Give the preparation type.
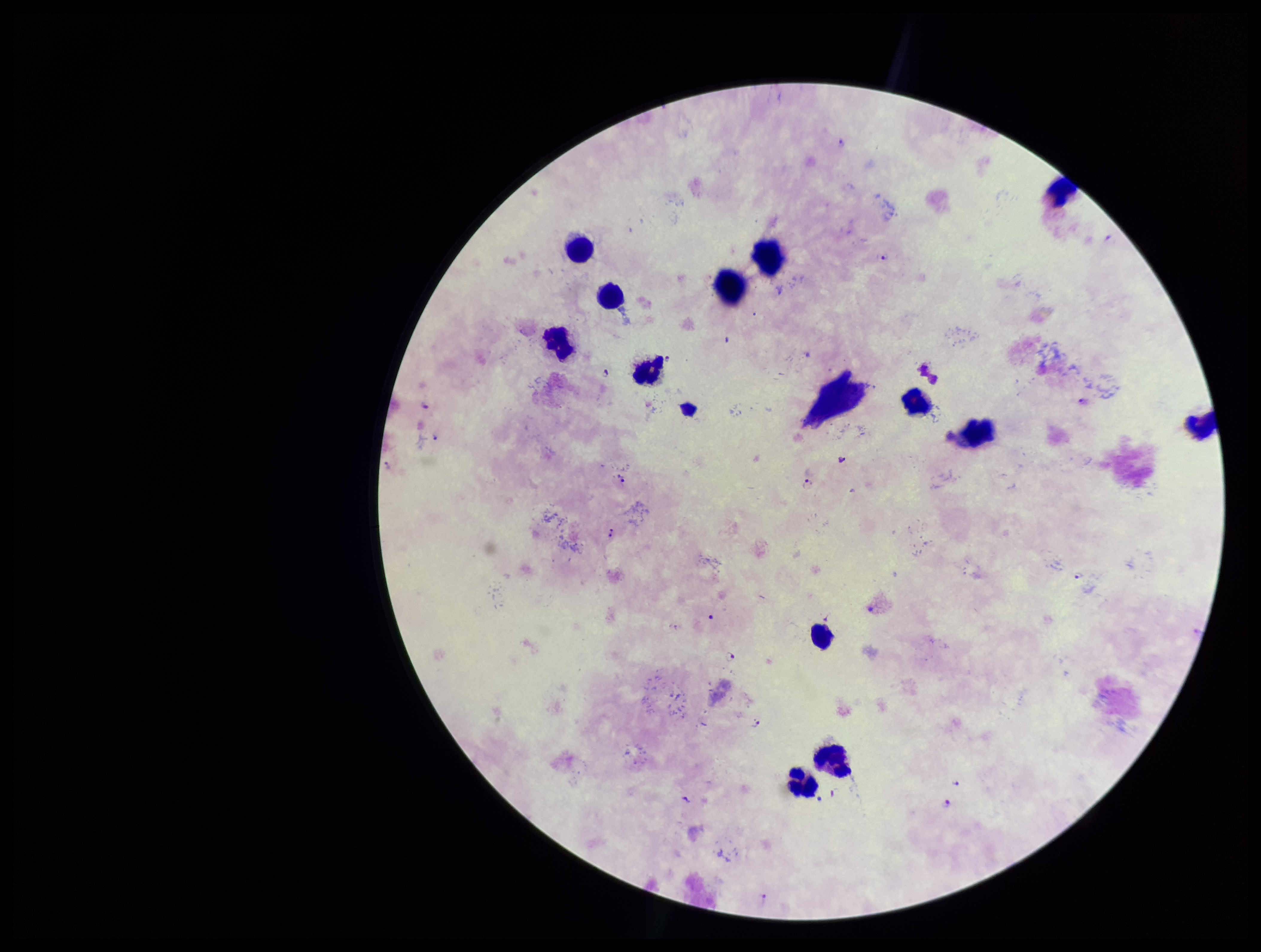
It is a thick blood smear.

Stained with Giemsa. Image is 1261×952 pixels. Single field of view. Parasite count: 19. Plasmodium parasites: seen. Leukocyte count: 12. Photographed through the microscope eyepiece with a smartphone camera. Species reported for this patient: Plasmodium falciparum. Patient malaria status: positive.